Assess this cell for malaria.
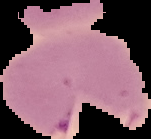
Uninfected.

The area outside the segmented cell region is set to black. Image is 151×139 pixels. From a thin blood film.